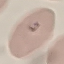
Malaria status: parasitized. Automatically extracted cell patch, resized to 64 × 64 pixels. Photographed with a smartphone camera at the microscope eyepiece. Thin blood film. Giemsa stain.